Assess this cell for malaria.
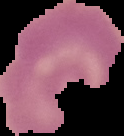
It is uninfected.

image size = 124×136 pixels
image type = cell region segmented out of the field of view; surrounding area masked to black
preparation = thin blood film